Locate every Plasmodium parasite.
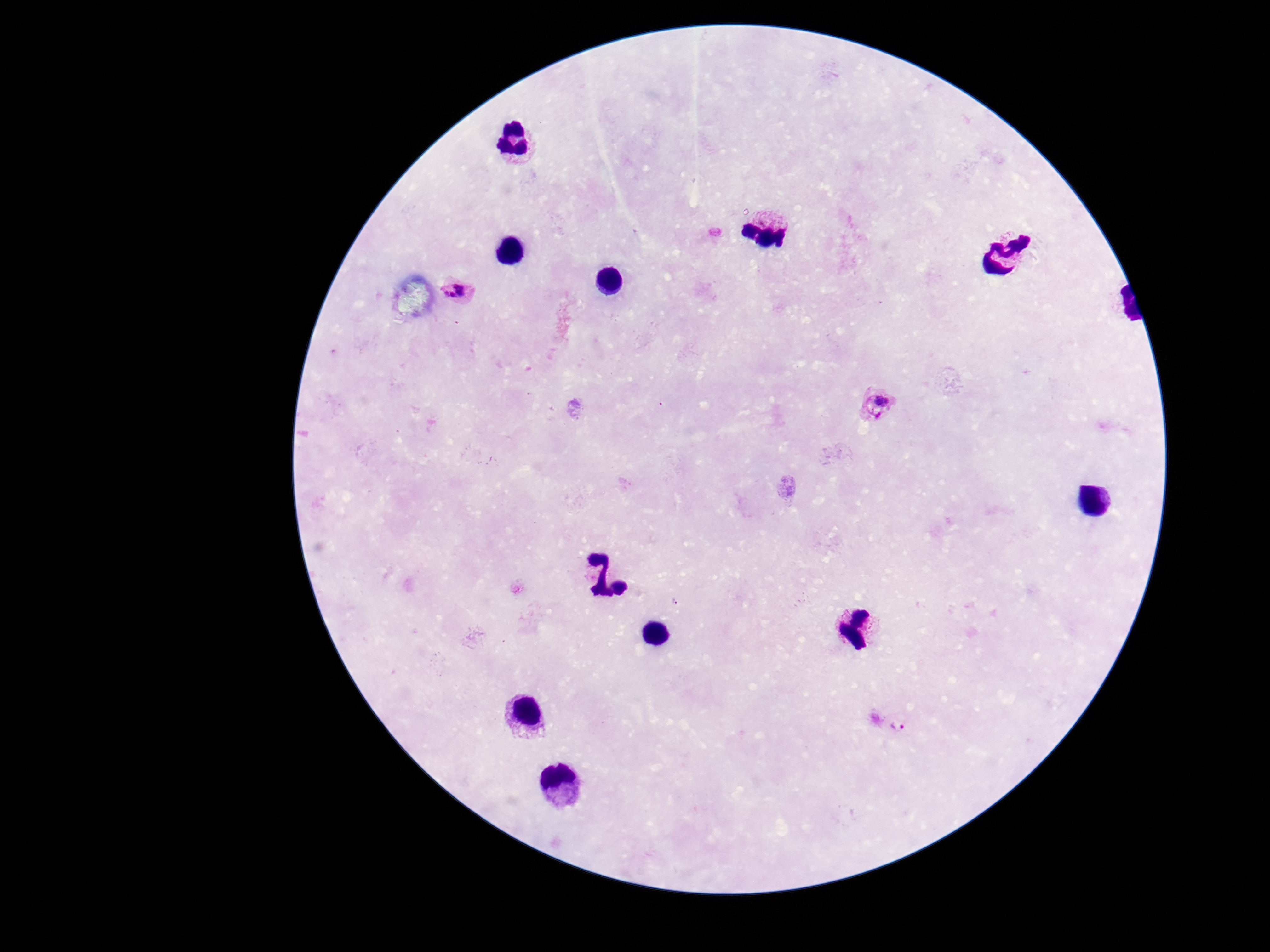
Approximate object centers, in pixels from the top-left corner.
Plasmodium parasites: (x=461, y=290), (x=881, y=405), (x=896, y=723).

Image is 1270×952 pixels. 100x magnification. Patient malaria status: positive. Thick peripheral-blood smear. One field from this slide. Photographed through the microscope eyepiece with a smartphone camera. Giemsa-stained preparation.